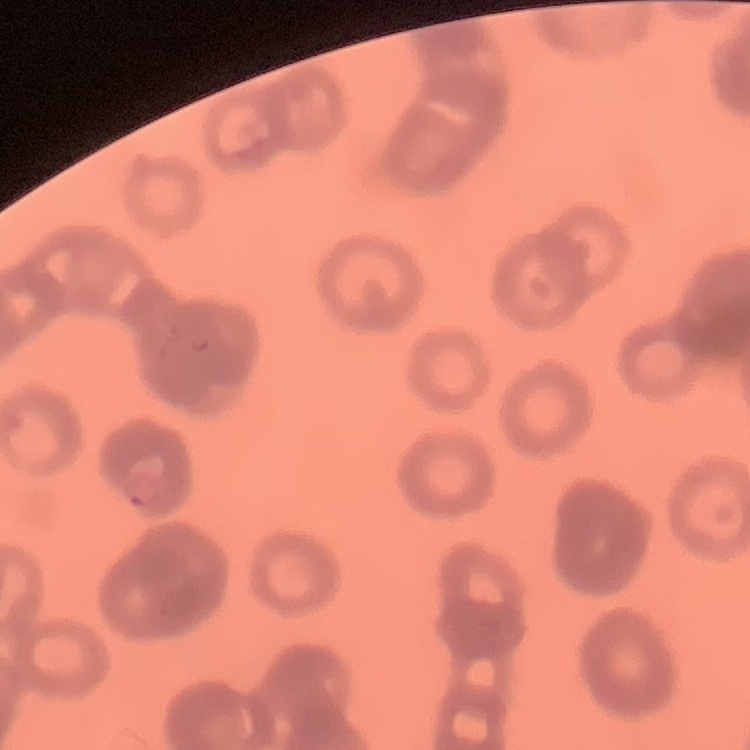
The erythrocytes exhibit rouleaux formation. Thin peripheral smear. Stained with either Field's or Giemsa. Square crop of a larger photomicrograph.